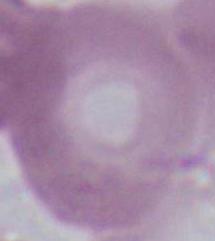 Captured at 1000x magnification. Photomicrograph. An erythrocyte is seen.